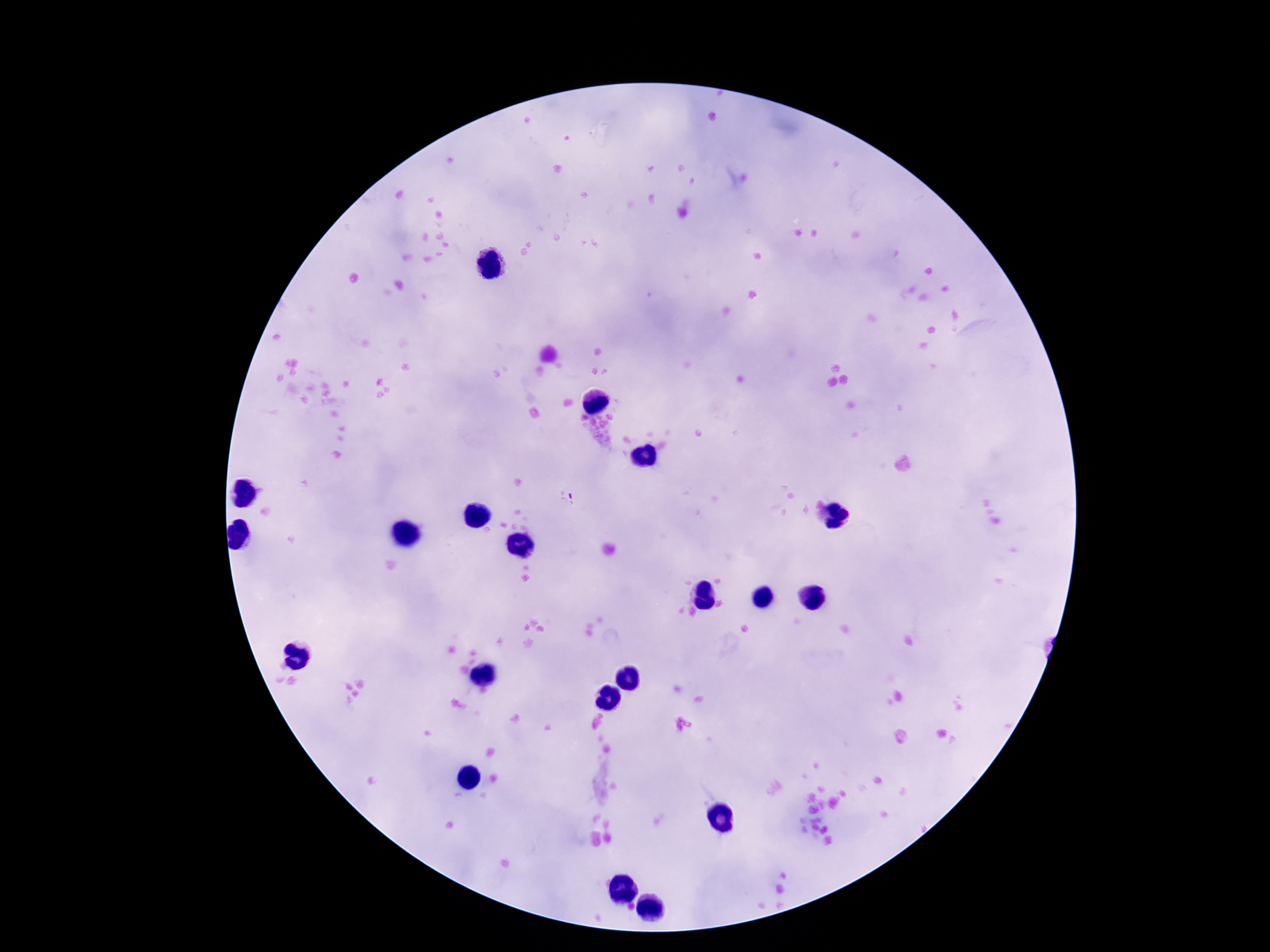

Approximate centers as [x, y] in pixels.
Summary:
  - Plasmodium parasite locations: [566, 499]
  - Capture: smartphone camera through the microscope eyepiece
  - Image size: 1270×952 pixels
  - Stain: Giemsa
  - Patient malaria status: infected
  - Magnification: 100x
  - Field of view: single
  - Preparation: thick blood smear